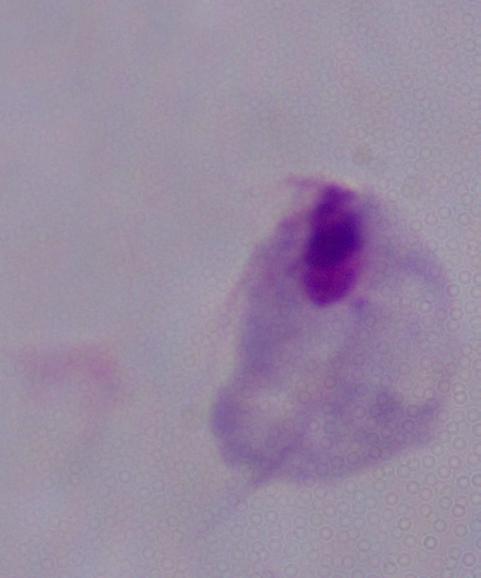
Summary:
  - Identification: trichomonad
  - Magnification: 1000x
  - Modality: photomicrograph